Assess this cell for malaria.
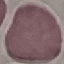
Uninfected.

Summary:
  - Capture: smartphone camera at the microscope eyepiece
  - Preparation: thin smear
  - Image type: cell patch, automatically extracted from a larger field of view and resized to 64 × 64 pixels
  - Stain: Giemsa